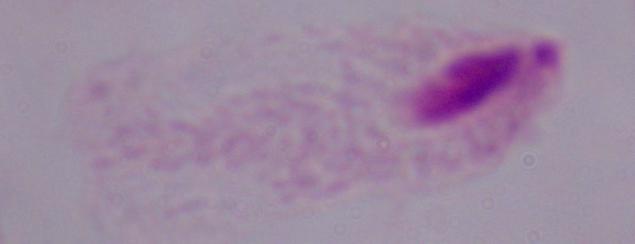

Captured at 1000x magnification. Photomicrograph. A trichomonad is seen.